Comment on the morphology of the erythrocytes.
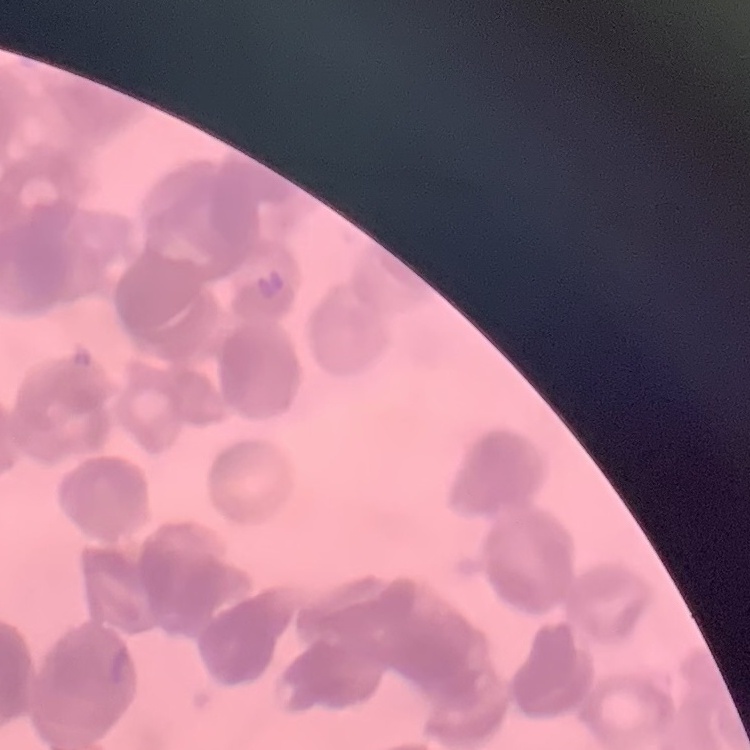
Rouleaux formation.

Thin blood film. Stained with either Field's or Giemsa. One tile cut from a larger photomicrograph.